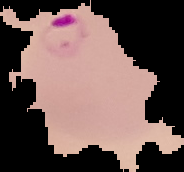
Summary:
  - Result: Plasmodium parasites identified
  - Image type: segmented cell region with the area outside set to black
  - Preparation: thin blood smear
  - Image size: 184×172 pixels